State the blood parasite species.
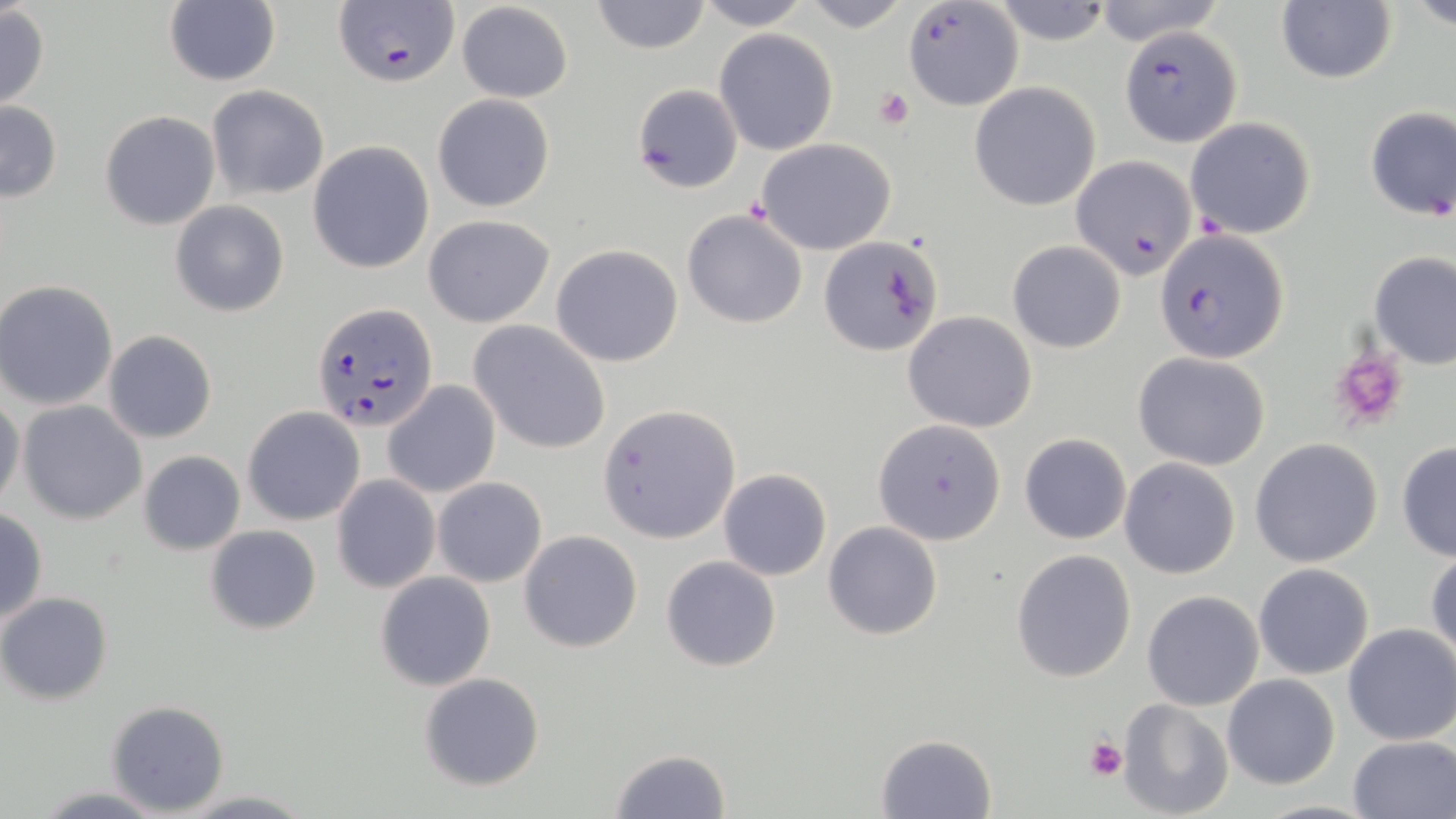

Plasmodium falciparum.

Summary:
  - Coordinate format: approximate bounding boxes as (x1, y1, x2, y2) in pixels
  - Plasmodium falciparum-infected red blood cell locations: (333, 0, 459, 87), (902, 1, 1023, 111), (1121, 26, 1242, 146), (1073, 156, 1200, 279), (1158, 231, 1288, 363), (311, 301, 439, 433)
  - Uninfected red blood cell locations: (164, 0, 281, 86), (591, 0, 710, 53), (689, 0, 815, 30), (796, 0, 913, 31), (1088, 0, 1224, 47), (1410, 0, 1456, 30), (455, 1, 574, 103), (991, 1, 1113, 45), (1274, 3, 1396, 85), (0, 5, 50, 110), (715, 31, 838, 157), (969, 81, 1103, 211), (630, 82, 744, 195), (205, 86, 329, 200), (432, 94, 555, 212), (0, 101, 62, 201), (1362, 105, 1456, 223), (99, 110, 220, 230), (1184, 116, 1317, 239), (756, 137, 898, 255), (307, 142, 435, 273), (169, 200, 289, 317), (682, 209, 809, 328), (424, 214, 555, 328), (821, 236, 945, 356), (1007, 241, 1126, 353), (552, 244, 684, 367), (1369, 250, 1456, 370), (1, 281, 119, 411), (903, 312, 1037, 433), (469, 320, 611, 455), (102, 330, 217, 444), (1135, 352, 1270, 470), (384, 381, 500, 498), (0, 394, 25, 515), (18, 401, 147, 523), (598, 403, 739, 542), (243, 407, 364, 524), (873, 420, 1005, 546), (1019, 432, 1132, 544), (1249, 438, 1383, 569), (1396, 442, 1456, 561), (138, 451, 245, 555), (1119, 457, 1239, 579), (718, 468, 832, 581), (332, 474, 439, 595), (433, 476, 547, 587), (0, 509, 48, 626), (823, 521, 943, 640), (205, 524, 322, 635), (518, 529, 644, 652), (1426, 545, 1456, 668), (1011, 549, 1138, 684), (661, 556, 782, 672), (1253, 563, 1375, 681), (374, 571, 497, 692), (1142, 590, 1264, 711), (0, 592, 114, 704), (1343, 623, 1456, 746), (418, 672, 545, 791), (1222, 673, 1340, 789), (1117, 698, 1234, 819), (105, 699, 231, 815), (875, 733, 997, 819), (1348, 733, 1456, 817), (608, 748, 732, 819), (28, 785, 173, 817), (177, 791, 316, 817)
  - Platelet locations: (871, 86, 914, 129), (1329, 342, 1413, 431), (1085, 735, 1128, 781)
  - Preparation: thin blood smear
  - Modality: optical microscopy
  - Magnification: 1000x
  - Stain: May-Grünwald-Giemsa
  - Field of view: single
  - Image size: 1456×819 pixels